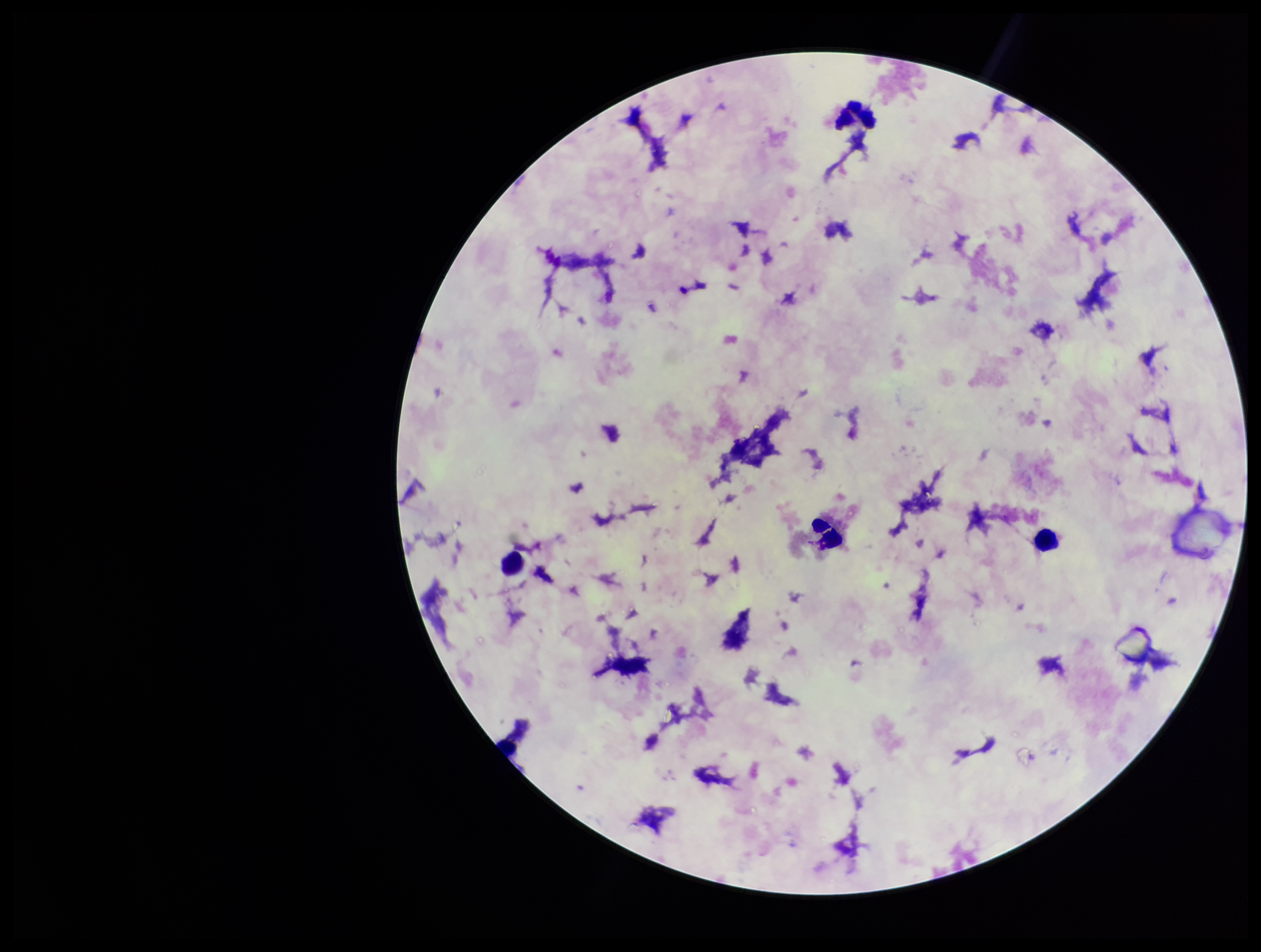

Stained with Giemsa. Plasmodium parasites: none identified. Patient malaria status: negative. One field from this slide. Preparation: thick blood smear. Smartphone photograph taken through the eyepiece of a microscope. Leukocyte count: 4. Parasite count: 0. Image is 1261×952 pixels.